State the blood parasite species.
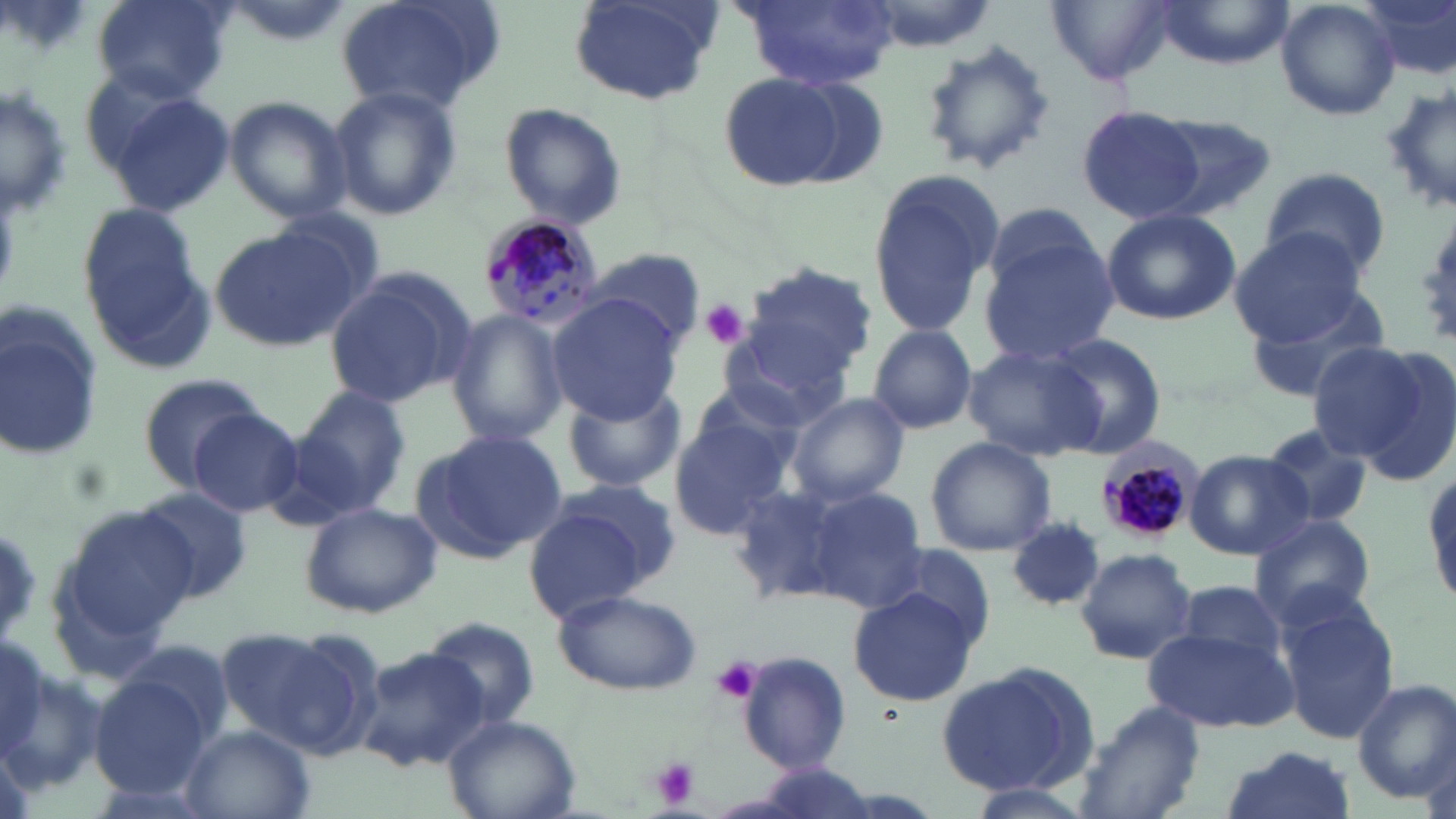

Plasmodium malariae.

Summary:
  - Coordinate format: approximate bounding boxes as (x1,y1)-(x2,y2) corner pairs in pixels
  - Plasmodium malariae-infected red blood cell locations: (478,212)-(605,332), (1095,438)-(1203,547)
  - Platelet locations: (699,299)-(749,349), (709,656)-(763,705), (649,757)-(701,809)
  - Uninfected red blood cell locations: (90,0)-(230,102), (214,0)-(356,45), (332,0)-(505,117), (735,0)-(900,90), (850,0)-(1002,50), (1153,0)-(1292,68), (1274,0)-(1401,122), (1360,0)-(1456,83), (568,1)-(724,108), (1048,1)-(1178,86), (916,39)-(1055,178), (714,69)-(862,194), (1,82)-(72,219), (1383,82)-(1456,220), (329,85)-(462,221), (110,91)-(234,216), (224,95)-(353,223), (498,102)-(628,230), (1075,103)-(1209,226), (1145,114)-(1279,220), (866,166)-(1003,339), (1260,166)-(1390,280), (74,202)-(210,365), (1101,208)-(1241,324), (979,218)-(1119,366), (205,226)-(362,353), (1228,228)-(1366,345), (584,247)-(707,349), (743,262)-(879,384), (324,267)-(475,411), (1241,284)-(1395,403), (546,295)-(683,421), (0,309)-(103,464), (445,309)-(569,448), (867,324)-(978,435), (718,328)-(850,434), (1044,333)-(1168,458), (1303,339)-(1441,464), (964,342)-(1105,462), (135,372)-(267,486), (558,380)-(688,493), (295,386)-(411,511), (786,392)-(909,506), (669,405)-(800,537), (188,407)-(308,516), (1259,425)-(1378,530), (411,431)-(566,562), (923,437)-(1056,556), (1186,450)-(1313,560), (726,480)-(863,609), (135,486)-(252,601), (799,486)-(928,611), (522,492)-(664,618), (299,500)-(443,618), (52,503)-(200,655), (1248,512)-(1378,629), (1009,519)-(1105,612), (883,540)-(998,645), (1074,547)-(1197,665), (1175,579)-(1292,669), (551,588)-(701,695), (847,588)-(981,707), (1277,596)-(1400,747), (421,617)-(543,727), (1143,624)-(1298,735), (227,625)-(382,758), (356,646)-(489,772), (734,651)-(850,774), (934,665)-(1093,795), (89,669)-(216,800), (1352,680)-(1455,803), (1072,700)-(1207,819), (443,714)-(580,819), (178,723)-(317,819), (1217,745)-(1355,819), (963,782)-(1098,819)
  - Modality: optical microscopy
  - Magnification: 1000x
  - Field of view: single
  - Stain: May-Grünwald-Giemsa
  - Image size: 1456×819 pixels
  - Preparation: thin blood smear